Locate and identify every blood parasite.
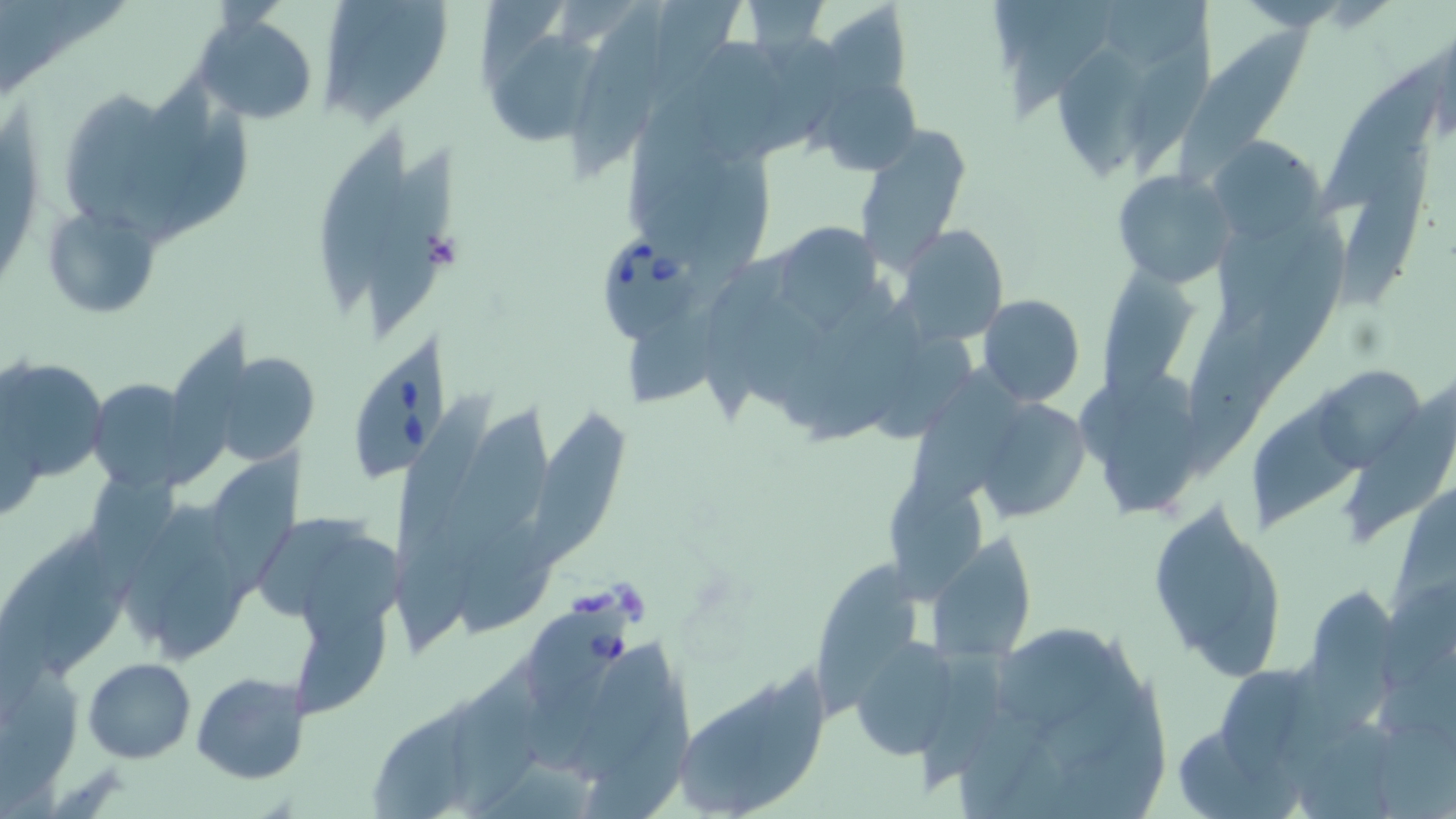

Approximate bounding boxes as [x1, y1, x2, y2] in pixels.
Babesia divergens-infected red blood cells: [598, 222, 713, 344], [349, 335, 457, 483], [518, 601, 635, 716].
No Plasmodium falciparum, Plasmodium ovale, Plasmodium malariae, Plasmodium vivax, or Trypanosoma brucei observed.

slide-level diagnosis = Babesia divergens
modality = light microscopy
magnification = 1000x
platelet locations = approximate bounding boxes as [x1, y1, x2, y2] in pixels: [423, 230, 463, 273]
image size = 1456×819 pixels
field of view = single
stain = May-Grünwald-Giemsa
uninfected red blood cell locations = approximate bounding boxes as [x1, y1, x2, y2] in pixels: [317, 0, 453, 126], [574, 1, 667, 178], [816, 2, 911, 102], [1006, 5, 1118, 118], [193, 13, 320, 125], [1178, 27, 1319, 182], [493, 28, 606, 145], [1056, 43, 1160, 176], [698, 44, 786, 166], [1316, 55, 1450, 208], [140, 70, 217, 242], [813, 72, 922, 179], [58, 89, 160, 226], [853, 125, 972, 273], [320, 130, 409, 306], [1209, 137, 1324, 241], [1331, 148, 1437, 307], [368, 152, 470, 332], [1112, 170, 1234, 285], [45, 206, 160, 316], [773, 217, 880, 328], [896, 224, 1009, 344], [1097, 259, 1197, 410], [976, 294, 1085, 407], [629, 311, 727, 404], [168, 327, 268, 483], [202, 346, 321, 467], [1, 355, 107, 483], [1316, 368, 1428, 477], [85, 378, 208, 492], [398, 395, 507, 562], [1253, 395, 1359, 533], [978, 396, 1092, 522], [444, 408, 562, 556], [521, 410, 631, 574], [217, 449, 317, 602], [881, 470, 990, 609], [1146, 495, 1289, 682], [112, 496, 264, 662], [259, 518, 382, 630], [42, 523, 144, 676], [931, 536, 1041, 659], [305, 537, 408, 646], [812, 568, 928, 720], [1301, 585, 1406, 713], [997, 626, 1118, 728], [850, 635, 966, 759], [576, 643, 682, 784], [0, 654, 83, 797], [82, 657, 196, 763], [451, 662, 554, 816], [192, 672, 308, 784], [679, 685, 790, 817], [582, 698, 701, 819], [368, 699, 488, 819]
preparation = thin blood film